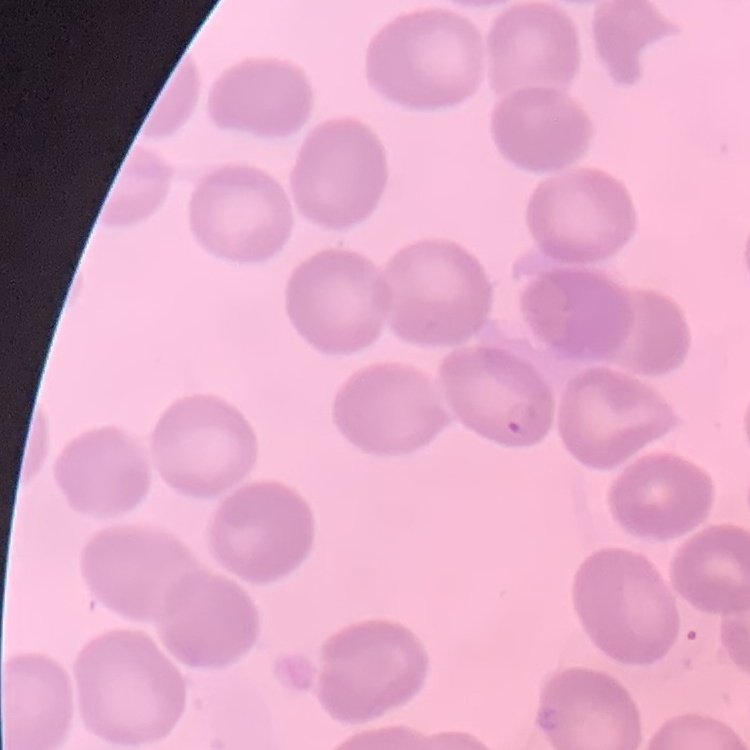

erythrocyte morphology = no rouleaux formation
preparation = thin blood smear
image type = one tile cut from a larger photomicrograph
stain = Field's or Giemsa